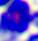
Summary:
  - Modality: photomicrograph
  - Identification: leukocyte
  - Magnification: 400x